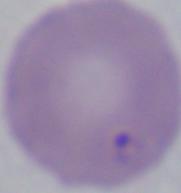
magnification = 1000x
modality = micrograph
identification = Babesia